Give the extent of all Plasmodium falciparum-infected red blood cells.
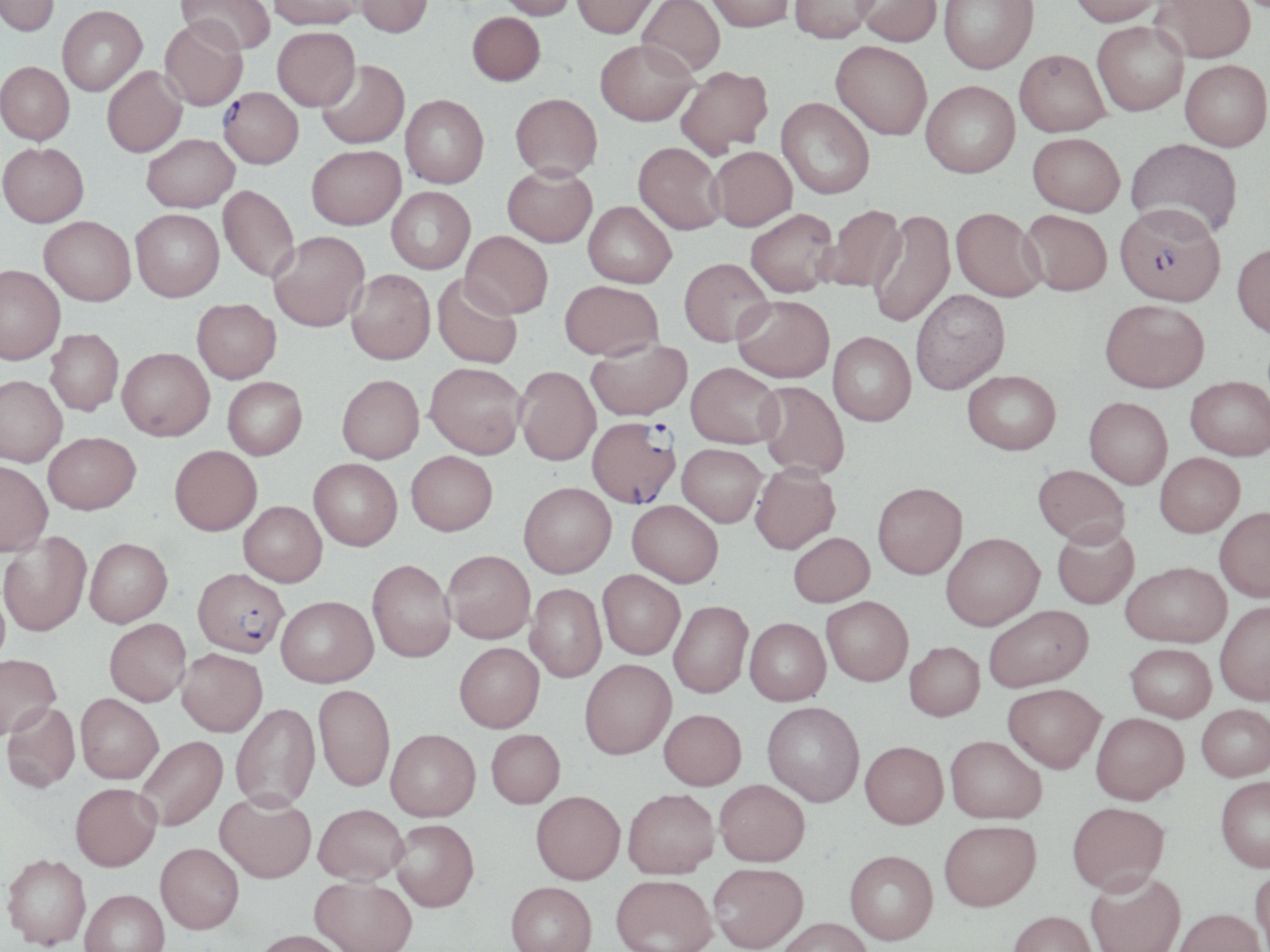
Approximate bounding boxes as [x1, y1, x2, y2] in pixels.
Plasmodium falciparum-infected red blood cells: [218, 90, 303, 172], [1118, 209, 1229, 314], [587, 421, 681, 511], [196, 569, 296, 660].

Summary:
  - Uninfected red blood cell locations: [0, 0, 59, 39], [176, 0, 274, 57], [269, 0, 363, 33], [356, 0, 432, 41], [494, 0, 577, 22], [572, 0, 659, 41], [637, 0, 725, 79], [706, 0, 793, 34], [789, 0, 880, 45], [855, 0, 942, 49], [939, 0, 1039, 76], [1070, 0, 1165, 30], [1150, 0, 1257, 66], [58, 8, 147, 98], [467, 15, 545, 89], [159, 23, 247, 113], [1092, 23, 1188, 118], [273, 31, 360, 114], [595, 43, 699, 129], [830, 44, 931, 143], [1014, 53, 1110, 140], [317, 62, 410, 151], [1179, 62, 1270, 154], [0, 64, 74, 148], [102, 68, 188, 160], [676, 68, 774, 160], [921, 85, 1020, 182], [401, 97, 488, 191], [510, 97, 602, 185], [776, 99, 874, 201], [1027, 136, 1124, 219], [142, 137, 239, 215], [1125, 140, 1242, 244], [0, 145, 89, 230], [633, 145, 725, 237], [306, 148, 406, 232], [710, 148, 797, 234], [503, 169, 597, 250], [218, 187, 299, 284], [387, 188, 475, 275], [583, 202, 676, 291], [820, 206, 908, 295], [868, 210, 956, 329], [951, 210, 1045, 304], [131, 211, 225, 305], [746, 211, 838, 300], [1020, 211, 1112, 298], [39, 220, 135, 309], [460, 232, 552, 320], [269, 233, 369, 335], [1232, 246, 1270, 342], [679, 258, 774, 349], [0, 268, 65, 368], [346, 271, 435, 367], [432, 276, 523, 370], [559, 282, 663, 363], [911, 291, 1010, 396], [733, 296, 835, 384], [1099, 300, 1209, 395], [192, 301, 281, 386], [45, 331, 123, 417], [827, 333, 916, 427], [586, 341, 693, 424], [116, 350, 214, 444], [425, 364, 526, 461], [686, 365, 783, 451], [515, 368, 601, 467], [962, 372, 1060, 456], [0, 377, 68, 468], [337, 377, 424, 465], [1185, 378, 1270, 462], [223, 379, 308, 462], [755, 382, 849, 480], [1083, 399, 1172, 490], [43, 433, 140, 516], [169, 446, 263, 538], [677, 446, 766, 529], [405, 452, 497, 538], [1155, 454, 1245, 540], [309, 460, 402, 553], [0, 462, 52, 559], [750, 467, 841, 557], [1032, 467, 1131, 553], [518, 485, 617, 581], [873, 486, 967, 583], [239, 503, 327, 588], [626, 503, 722, 590], [1215, 510, 1270, 605], [1052, 528, 1139, 611], [0, 533, 91, 637], [789, 535, 875, 610], [941, 536, 1045, 634], [84, 539, 172, 628], [443, 551, 535, 646], [367, 560, 456, 663], [1122, 565, 1231, 651], [598, 572, 684, 660], [525, 585, 606, 683], [276, 596, 378, 688], [821, 600, 913, 688], [669, 603, 752, 700], [1215, 603, 1270, 707], [985, 608, 1094, 695], [105, 618, 191, 707], [745, 620, 831, 708], [455, 643, 545, 734], [904, 644, 985, 724], [1125, 646, 1216, 725], [176, 649, 267, 738], [0, 655, 61, 739], [580, 661, 676, 762], [313, 685, 394, 792], [1002, 686, 1104, 776], [76, 694, 163, 785], [2, 703, 80, 794], [230, 704, 321, 813], [762, 704, 864, 809], [1197, 706, 1270, 783], [659, 712, 745, 792], [1091, 715, 1188, 808], [386, 730, 480, 823], [486, 731, 565, 810], [137, 736, 228, 832], [945, 739, 1046, 827], [860, 744, 948, 832], [1216, 779, 1270, 874], [715, 781, 810, 869], [70, 783, 162, 871], [623, 791, 719, 881], [530, 792, 625, 886], [215, 794, 316, 884], [313, 804, 408, 886], [1068, 804, 1171, 898], [390, 820, 479, 912], [939, 824, 1041, 915], [155, 843, 243, 934], [845, 853, 938, 947], [2, 854, 90, 949], [708, 864, 809, 952], [1250, 869, 1270, 951], [1086, 874, 1186, 952], [309, 877, 417, 952], [611, 877, 716, 952], [506, 883, 597, 952], [79, 890, 170, 952], [1173, 912, 1267, 952], [1008, 914, 1097, 952], [776, 919, 873, 952], [250, 930, 350, 952]
  - Slide-level diagnosis: Plasmodium falciparum
  - Preparation: thin blood smear
  - Image size: 1270×952 pixels
  - Modality: optical microscopy
  - Field of view: single
  - Magnification: 1000x
  - Stain: May-Grünwald-Giemsa